State the blood parasite species.
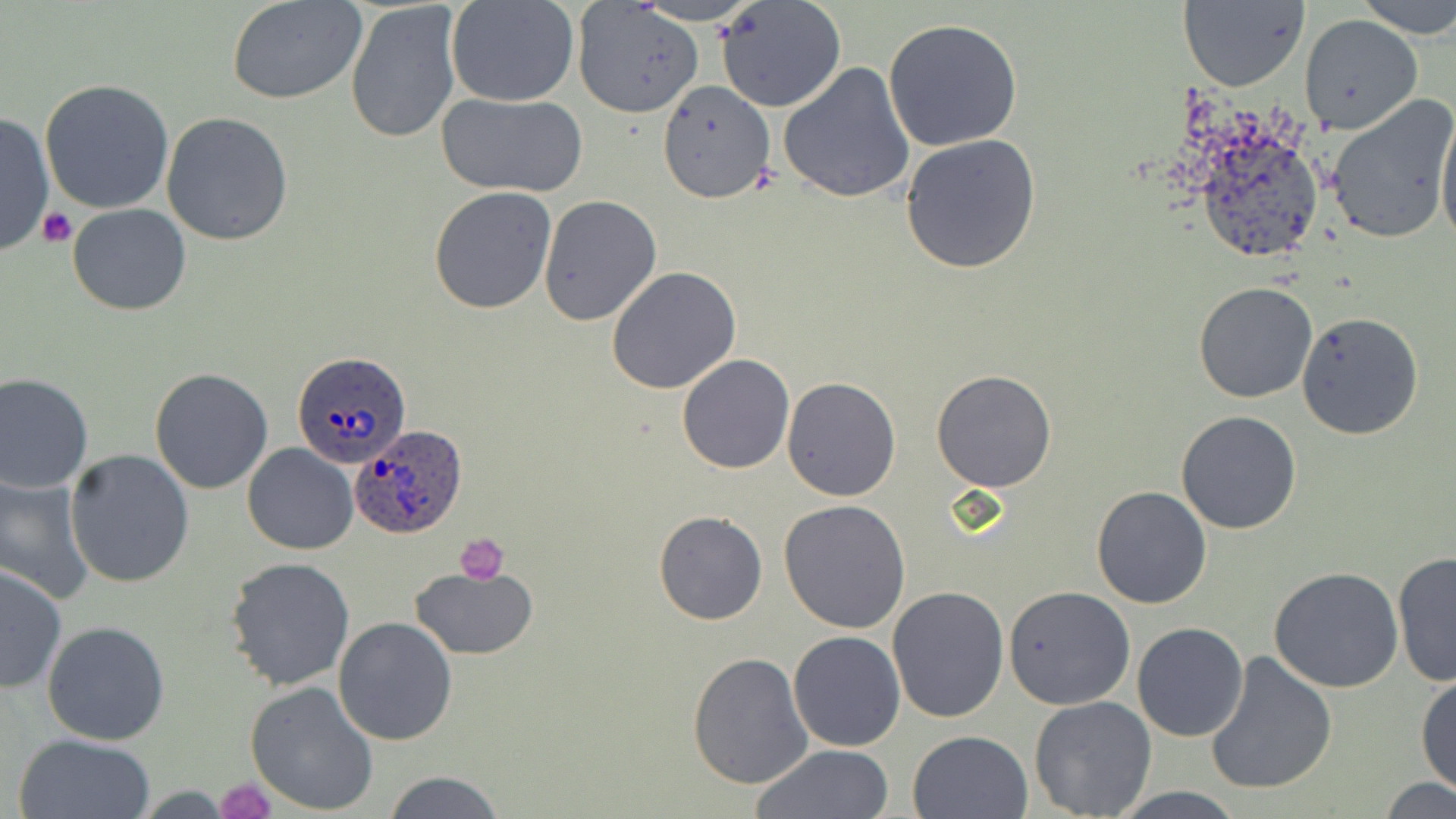

Plasmodium ovale.

Approximate bounding boxes as named x1/y1/x2/y2 corners in pixels. Platelet locations: (x1=39, y1=207, x2=77, y2=249), (x1=454, y1=533, x2=509, y2=583), (x1=215, y1=777, x2=276, y2=818). Uninfected red blood cell locations: (x1=226, y1=0, x2=370, y2=104), (x1=447, y1=0, x2=580, y2=107), (x1=633, y1=0, x2=762, y2=26), (x1=716, y1=0, x2=846, y2=112), (x1=1179, y1=0, x2=1309, y2=92), (x1=1352, y1=0, x2=1456, y2=40), (x1=344, y1=1, x2=465, y2=145), (x1=573, y1=2, x2=705, y2=120), (x1=1299, y1=15, x2=1422, y2=135), (x1=881, y1=18, x2=1025, y2=153), (x1=777, y1=61, x2=916, y2=202), (x1=40, y1=79, x2=175, y2=215), (x1=657, y1=80, x2=778, y2=203), (x1=435, y1=91, x2=588, y2=197), (x1=1323, y1=94, x2=1456, y2=244), (x1=1436, y1=103, x2=1456, y2=252), (x1=0, y1=110, x2=54, y2=257), (x1=160, y1=112, x2=294, y2=245), (x1=1186, y1=114, x2=1329, y2=270), (x1=900, y1=134, x2=1041, y2=274), (x1=429, y1=186, x2=558, y2=315), (x1=537, y1=194, x2=663, y2=326), (x1=67, y1=203, x2=191, y2=316), (x1=607, y1=266, x2=741, y2=394), (x1=1193, y1=281, x2=1319, y2=404), (x1=1295, y1=310, x2=1425, y2=440), (x1=677, y1=355, x2=795, y2=475), (x1=149, y1=368, x2=274, y2=494), (x1=931, y1=370, x2=1058, y2=492), (x1=0, y1=372, x2=95, y2=495), (x1=781, y1=376, x2=902, y2=501), (x1=1176, y1=410, x2=1303, y2=534), (x1=242, y1=443, x2=357, y2=554), (x1=64, y1=448, x2=195, y2=588), (x1=0, y1=472, x2=95, y2=603), (x1=1091, y1=485, x2=1213, y2=609), (x1=779, y1=499, x2=912, y2=633), (x1=653, y1=511, x2=769, y2=626), (x1=1392, y1=551, x2=1456, y2=689), (x1=224, y1=556, x2=356, y2=690), (x1=0, y1=562, x2=67, y2=695), (x1=409, y1=565, x2=537, y2=662), (x1=1268, y1=567, x2=1403, y2=693), (x1=887, y1=586, x2=1011, y2=724), (x1=1004, y1=586, x2=1135, y2=710), (x1=333, y1=616, x2=458, y2=745), (x1=41, y1=620, x2=170, y2=744), (x1=1132, y1=622, x2=1249, y2=742), (x1=789, y1=631, x2=905, y2=751), (x1=687, y1=652, x2=813, y2=790), (x1=1204, y1=653, x2=1336, y2=796), (x1=1415, y1=671, x2=1456, y2=797), (x1=245, y1=680, x2=380, y2=815), (x1=1028, y1=696, x2=1156, y2=818), (x1=907, y1=729, x2=1033, y2=818), (x1=11, y1=733, x2=156, y2=819), (x1=750, y1=745, x2=895, y2=819), (x1=385, y1=771, x2=504, y2=819), (x1=1377, y1=778, x2=1456, y2=818), (x1=1104, y1=789, x2=1251, y2=819). Plasmodium ovale-infected red blood cell locations: (x1=293, y1=349, x2=414, y2=469), (x1=353, y1=424, x2=469, y2=538). Image is 1456×819 pixels. Light microscopy. Thin blood smear. Captured at 1000x magnification. One field of a larger specimen. May-Grünwald-Giemsa stain.